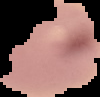
Summary:
  - Image size: 100×97 pixels
  - Image type: segmented cell region on a black background
  - Malaria status: uninfected
  - Preparation: thin blood smear